Classify this cell by malaria status.
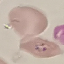

It is parasitized.

Giemsa stain. Cell patch, automatically extracted from a larger field of view and resized to 64 × 64 pixels. Photographed with a smartphone camera at the microscope eyepiece. Thin blood film.